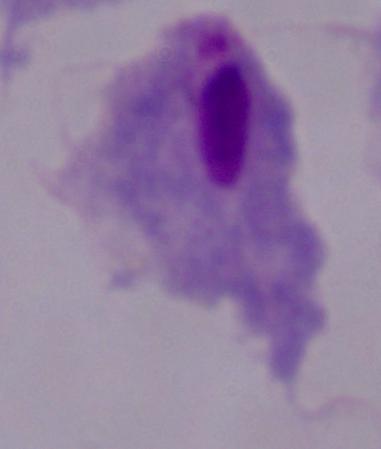
Summary:
  - Modality: photomicrograph
  - Identification: trichomonad
  - Magnification: 1000x